Point out each Plasmodium parasite.
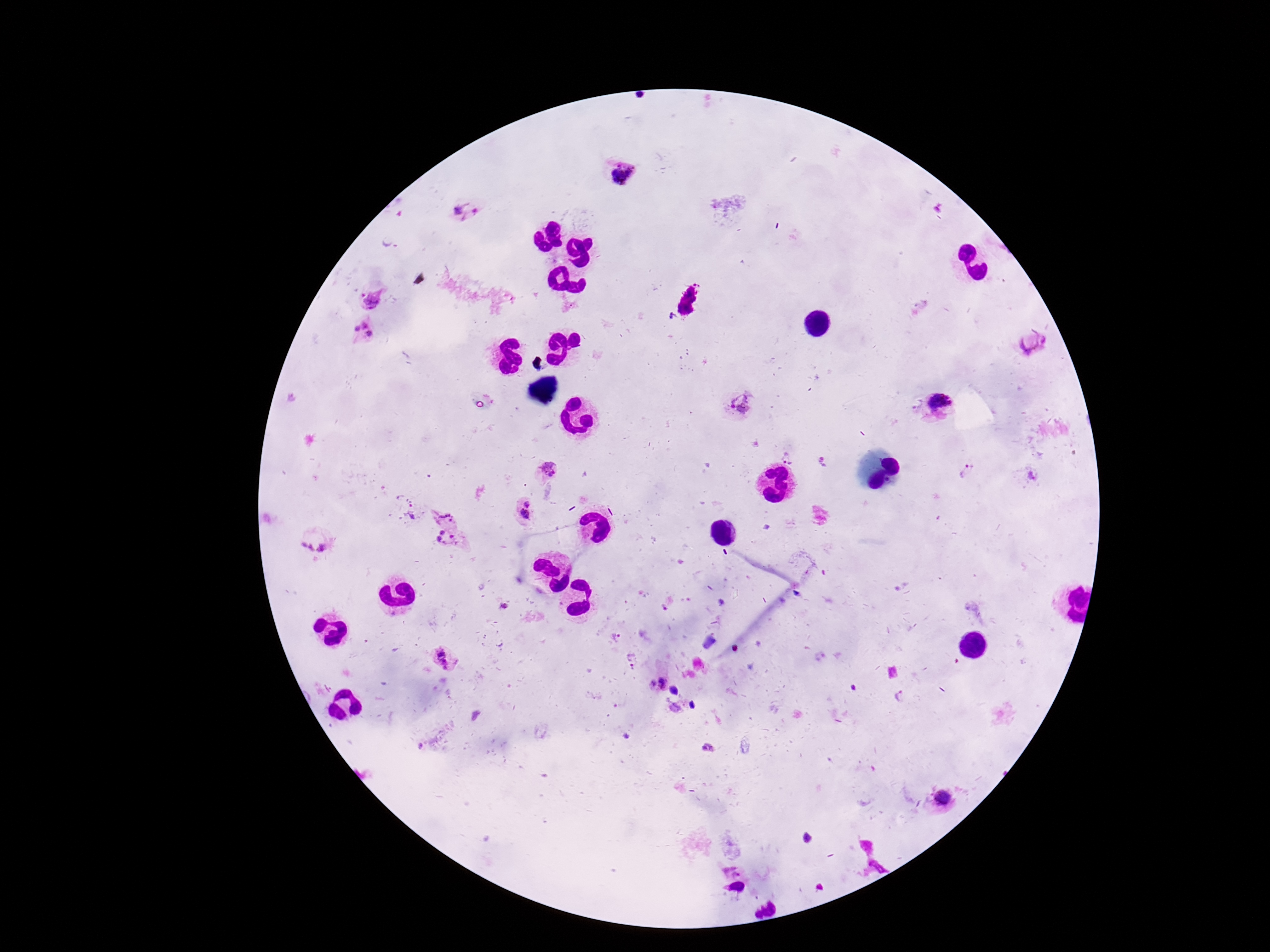

Approximate centers as (x, y) in pixels.
Plasmodium parasites: (618, 173), (460, 211), (370, 297), (362, 331), (1032, 343), (739, 405), (937, 406), (789, 454), (823, 461), (547, 469), (968, 471), (1033, 476), (525, 509), (412, 510), (446, 527), (315, 546), (504, 605), (616, 639), (443, 660), (632, 661), (658, 682), (710, 746), (944, 798), (808, 838).

Thick blood smear. 100x magnification. Patient malaria status: infected. Image is 1270×952 pixels. Smartphone photograph taken through the microscope eyepiece. Single field of view. Giemsa stain.